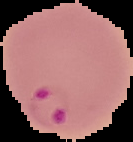 Result: malaria parasites identified. Cell region segmented out of the field of view; the surrounding area is masked to black. From a thin blood smear. Image is 133×142 pixels.